Locate and identify every blood parasite.
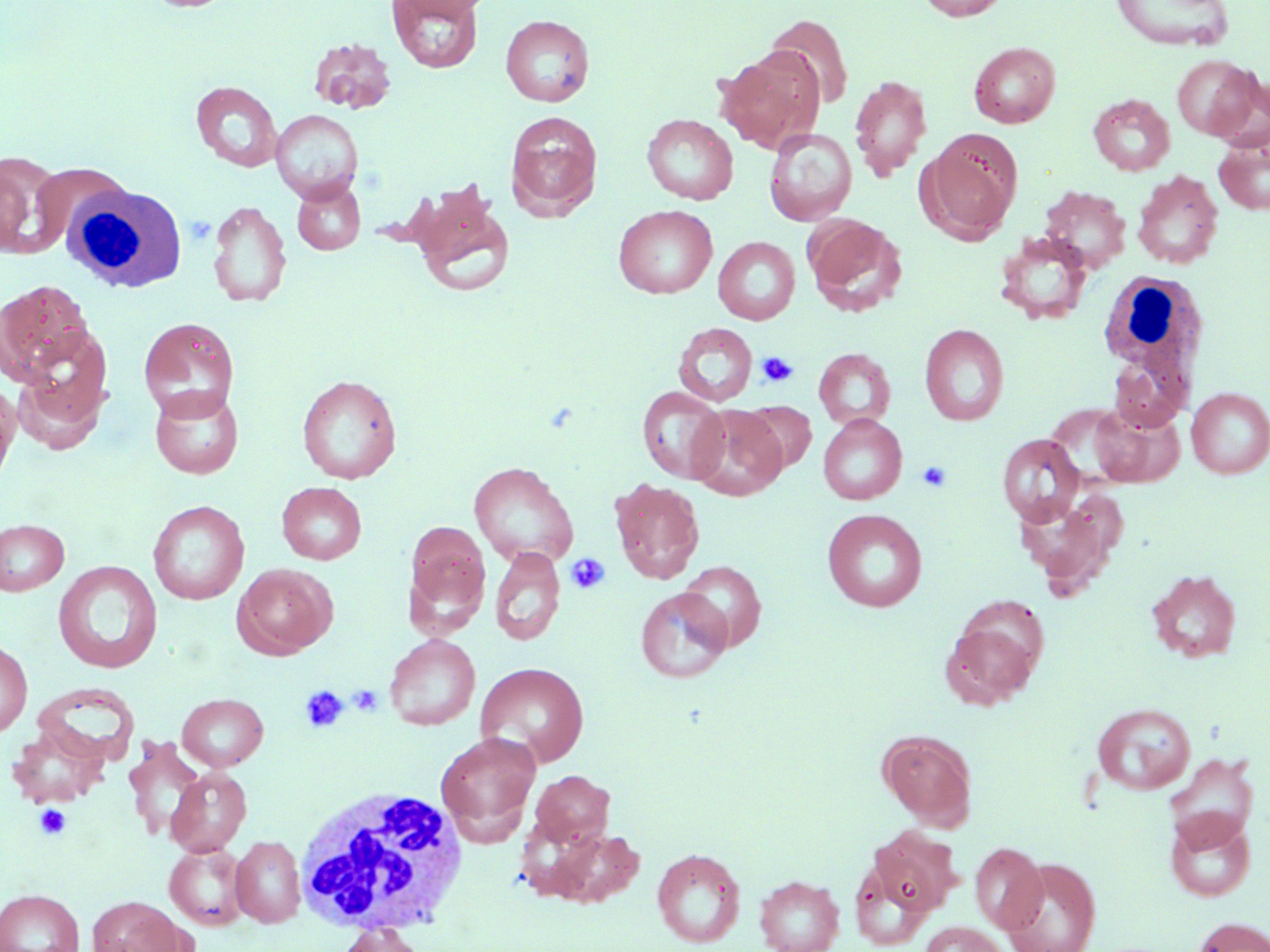
No blood parasites seen.

slide-level diagnosis = negative for blood parasites
uninfected red blood cell locations = approximate bounding boxes as named x1/y1/x2/y2 corners in pixels: (x1=143, y1=0, x2=240, y2=13), (x1=386, y1=0, x2=484, y2=73), (x1=393, y1=0, x2=497, y2=19), (x1=915, y1=0, x2=1011, y2=21), (x1=1110, y1=0, x2=1233, y2=51), (x1=500, y1=14, x2=595, y2=107), (x1=765, y1=15, x2=854, y2=109), (x1=309, y1=38, x2=396, y2=114), (x1=968, y1=42, x2=1060, y2=128), (x1=716, y1=48, x2=824, y2=152), (x1=1171, y1=54, x2=1260, y2=140), (x1=850, y1=75, x2=932, y2=180), (x1=1209, y1=76, x2=1270, y2=153), (x1=191, y1=81, x2=282, y2=171), (x1=1089, y1=94, x2=1175, y2=175), (x1=271, y1=109, x2=363, y2=202), (x1=504, y1=111, x2=602, y2=221), (x1=642, y1=114, x2=738, y2=204), (x1=764, y1=128, x2=857, y2=226), (x1=924, y1=130, x2=1022, y2=239), (x1=1213, y1=136, x2=1270, y2=215), (x1=0, y1=151, x2=68, y2=259), (x1=24, y1=161, x2=135, y2=253), (x1=1132, y1=170, x2=1224, y2=269), (x1=291, y1=178, x2=365, y2=255), (x1=407, y1=185, x2=516, y2=299), (x1=1038, y1=186, x2=1131, y2=272), (x1=207, y1=200, x2=291, y2=307), (x1=613, y1=205, x2=717, y2=298), (x1=802, y1=214, x2=908, y2=317), (x1=993, y1=231, x2=1093, y2=325), (x1=713, y1=236, x2=800, y2=325), (x1=0, y1=279, x2=95, y2=387), (x1=138, y1=317, x2=240, y2=420), (x1=674, y1=322, x2=758, y2=407), (x1=919, y1=323, x2=1009, y2=427), (x1=1108, y1=343, x2=1191, y2=432), (x1=11, y1=347, x2=112, y2=455), (x1=814, y1=348, x2=896, y2=430), (x1=296, y1=374, x2=402, y2=483), (x1=0, y1=381, x2=20, y2=491), (x1=149, y1=386, x2=245, y2=479), (x1=637, y1=387, x2=728, y2=483), (x1=1186, y1=387, x2=1270, y2=479), (x1=738, y1=401, x2=816, y2=474), (x1=1088, y1=403, x2=1183, y2=487), (x1=688, y1=405, x2=787, y2=501), (x1=818, y1=414, x2=907, y2=504), (x1=996, y1=433, x2=1085, y2=526), (x1=469, y1=462, x2=579, y2=569), (x1=609, y1=478, x2=705, y2=584), (x1=276, y1=482, x2=366, y2=564), (x1=1012, y1=490, x2=1125, y2=590), (x1=148, y1=500, x2=249, y2=605), (x1=822, y1=509, x2=928, y2=612), (x1=0, y1=519, x2=69, y2=596), (x1=404, y1=520, x2=491, y2=628), (x1=490, y1=546, x2=566, y2=646), (x1=53, y1=560, x2=163, y2=673), (x1=677, y1=560, x2=767, y2=651), (x1=232, y1=563, x2=337, y2=659), (x1=1146, y1=569, x2=1241, y2=662), (x1=636, y1=588, x2=733, y2=684), (x1=940, y1=613, x2=1043, y2=710), (x1=384, y1=634, x2=481, y2=731), (x1=0, y1=638, x2=32, y2=737), (x1=475, y1=662, x2=589, y2=768), (x1=177, y1=693, x2=268, y2=771), (x1=1091, y1=702, x2=1196, y2=794), (x1=7, y1=724, x2=109, y2=808), (x1=878, y1=729, x2=978, y2=829), (x1=436, y1=732, x2=542, y2=843), (x1=123, y1=736, x2=206, y2=840), (x1=1164, y1=752, x2=1259, y2=848), (x1=166, y1=767, x2=252, y2=856), (x1=529, y1=769, x2=616, y2=850), (x1=1165, y1=810, x2=1257, y2=902), (x1=530, y1=824, x2=646, y2=910), (x1=867, y1=827, x2=961, y2=918), (x1=231, y1=835, x2=305, y2=928), (x1=164, y1=842, x2=251, y2=930), (x1=970, y1=843, x2=1047, y2=933), (x1=652, y1=848, x2=746, y2=948), (x1=1000, y1=857, x2=1102, y2=952), (x1=754, y1=875, x2=844, y2=952), (x1=1, y1=889, x2=84, y2=952), (x1=87, y1=896, x2=190, y2=952), (x1=1190, y1=917, x2=1270, y2=952), (x1=918, y1=921, x2=1010, y2=952), (x1=334, y1=922, x2=427, y2=952)
field of view = one of a larger specimen
preparation = thin blood film
image size = 1270×952 pixels
modality = optical microscopy
white blood cell locations = approximate bounding boxes as named x1/y1/x2/y2 corners in pixels: (x1=68, y1=183, x2=188, y2=293), (x1=1099, y1=269, x2=1209, y2=408), (x1=294, y1=785, x2=470, y2=936)
magnification = 1000x
platelet locations = approximate bounding boxes as named x1/y1/x2/y2 corners in pixels: (x1=186, y1=216, x2=215, y2=245), (x1=757, y1=351, x2=798, y2=387), (x1=917, y1=460, x2=953, y2=493), (x1=565, y1=552, x2=611, y2=595), (x1=299, y1=685, x2=350, y2=733), (x1=348, y1=685, x2=384, y2=716), (x1=34, y1=803, x2=71, y2=839)
stain = May-Grünwald-Giemsa